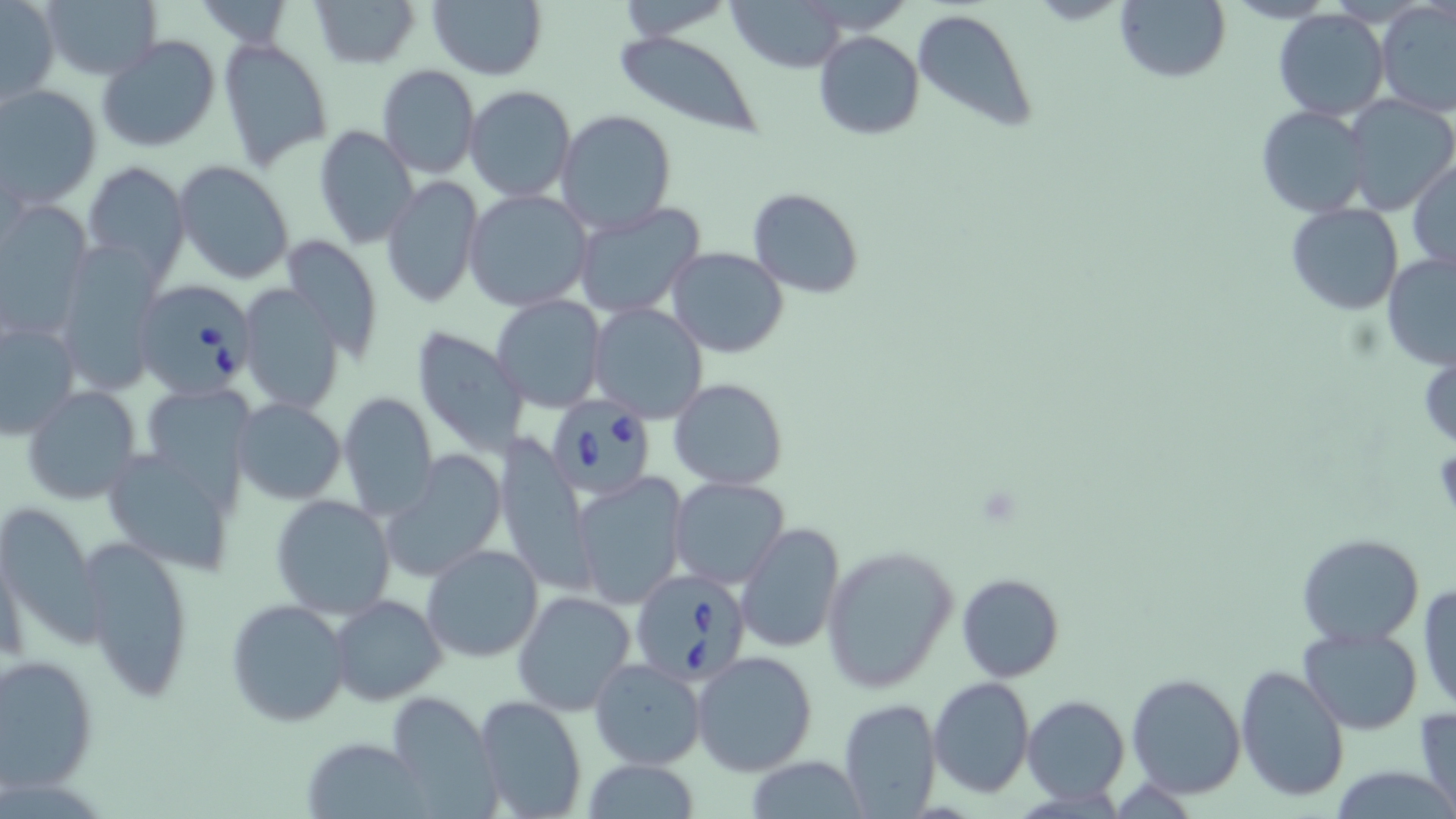
{
  "babesia_divergens_infected_red_blood_cell_locations": "approximate bounding boxes as [x1, y1, x2, y2] in pixels: [137, 280, 255, 400], [544, 392, 657, 499], [630, 566, 751, 685]",
  "slide_level_diagnosis": "Babesia divergens",
  "image_size": "1456×819 pixels",
  "uninfected_red_blood_cell_locations": "approximate bounding boxes as [x1, y1, x2, y2] in pixels: [308, 0, 419, 68], [1115, 0, 1230, 83], [1, 1, 59, 107], [39, 1, 160, 83], [427, 1, 547, 79], [610, 1, 739, 39], [729, 2, 848, 72], [1377, 3, 1456, 117], [911, 7, 1038, 133], [1273, 8, 1390, 122], [814, 31, 925, 140], [612, 32, 766, 138], [97, 35, 221, 153], [218, 37, 333, 170], [376, 65, 480, 180], [465, 85, 576, 201], [0, 86, 104, 211], [1343, 95, 1456, 214], [1255, 105, 1375, 218], [553, 109, 678, 236], [315, 124, 420, 250], [174, 160, 296, 284], [1408, 160, 1456, 272], [82, 161, 189, 284], [381, 176, 483, 309], [748, 189, 864, 298], [463, 190, 593, 311], [0, 200, 91, 338], [572, 203, 706, 320], [1285, 203, 1404, 315], [281, 234, 383, 363], [52, 244, 160, 394], [666, 248, 788, 357], [1381, 252, 1456, 373], [239, 284, 346, 414], [490, 294, 608, 413], [587, 302, 708, 422], [0, 317, 79, 440], [412, 326, 528, 459], [669, 378, 787, 490], [137, 383, 260, 504], [21, 384, 144, 507], [338, 392, 438, 518], [231, 398, 346, 504], [496, 435, 592, 591], [100, 446, 240, 574], [379, 451, 507, 583], [572, 472, 688, 609], [668, 477, 790, 590], [269, 493, 397, 620], [0, 501, 104, 645], [736, 523, 844, 652], [1297, 533, 1425, 645], [77, 535, 196, 701], [422, 543, 543, 663], [822, 544, 958, 694], [956, 572, 1064, 683], [1417, 580, 1456, 713], [512, 590, 636, 715], [331, 594, 446, 706], [225, 598, 353, 727], [1299, 626, 1424, 733], [692, 651, 819, 777], [1, 652, 99, 792], [588, 658, 706, 769], [1235, 664, 1350, 803], [1126, 672, 1246, 799], [927, 675, 1036, 801], [387, 691, 500, 817], [473, 693, 588, 818], [1023, 695, 1130, 805], [838, 698, 942, 818], [1415, 704, 1456, 819], [300, 735, 432, 818], [742, 758, 873, 817], [580, 759, 701, 817]",
  "field_of_view": "single",
  "stain": "May-Grünwald-Giemsa",
  "modality": "light microscopy",
  "preparation": "thin blood smear",
  "magnification": "1000x"
}